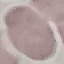

{
  "malaria_status": "uninfected",
  "image_type": "cell patch, automatically extracted from a larger field of view and resized to 64 × 64 pixels",
  "capture": "smartphone through the microscope eyepiece",
  "stain": "Giemsa",
  "preparation": "thin blood film"
}